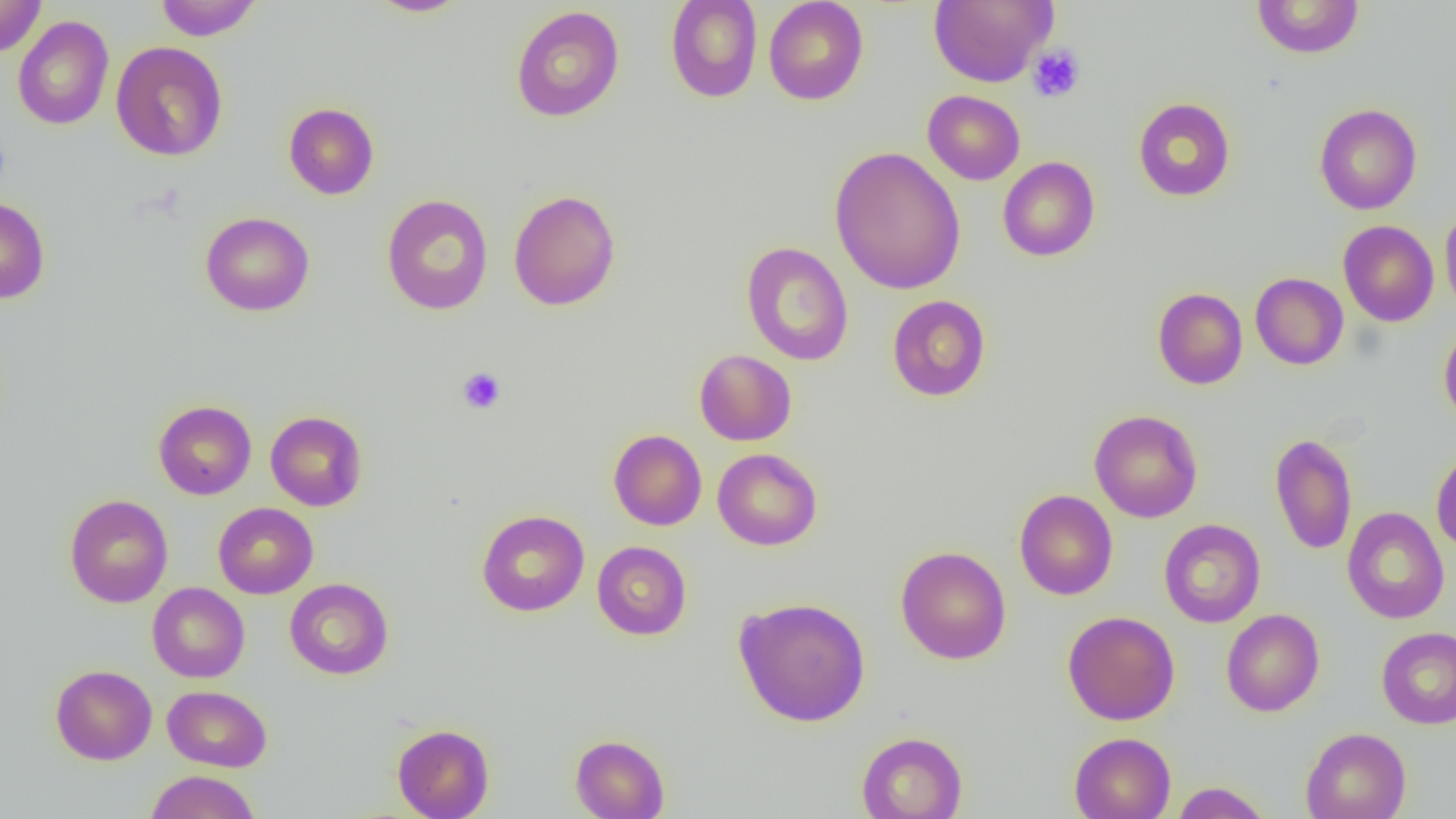
Summary:
  - Coordinate format: approximate bounding boxes as named x1/y1/x2/y2 corners in pixels
  - Uninfected red blood cell locations: (x1=0, y1=0, x2=46, y2=57), (x1=155, y1=0, x2=261, y2=41), (x1=365, y1=0, x2=472, y2=17), (x1=665, y1=0, x2=762, y2=103), (x1=763, y1=0, x2=869, y2=105), (x1=928, y1=0, x2=1057, y2=87), (x1=1251, y1=0, x2=1365, y2=59), (x1=510, y1=5, x2=625, y2=122), (x1=13, y1=15, x2=114, y2=129), (x1=110, y1=41, x2=228, y2=161), (x1=923, y1=90, x2=1025, y2=184), (x1=1133, y1=97, x2=1235, y2=202), (x1=283, y1=102, x2=379, y2=200), (x1=1314, y1=103, x2=1422, y2=214), (x1=829, y1=147, x2=966, y2=294), (x1=998, y1=157, x2=1100, y2=261), (x1=508, y1=189, x2=621, y2=311), (x1=381, y1=194, x2=494, y2=315), (x1=0, y1=197, x2=50, y2=304), (x1=1440, y1=203, x2=1456, y2=319), (x1=200, y1=212, x2=315, y2=316), (x1=1338, y1=220, x2=1439, y2=326), (x1=740, y1=241, x2=854, y2=366), (x1=1250, y1=272, x2=1348, y2=370), (x1=1152, y1=287, x2=1248, y2=389), (x1=887, y1=295, x2=991, y2=401), (x1=1439, y1=321, x2=1456, y2=426), (x1=694, y1=349, x2=797, y2=446), (x1=153, y1=400, x2=256, y2=500), (x1=1088, y1=409, x2=1203, y2=522), (x1=265, y1=411, x2=367, y2=511), (x1=608, y1=429, x2=707, y2=530), (x1=1269, y1=433, x2=1358, y2=555), (x1=712, y1=448, x2=822, y2=551), (x1=1431, y1=448, x2=1456, y2=555), (x1=1014, y1=489, x2=1118, y2=600), (x1=64, y1=494, x2=174, y2=608), (x1=213, y1=502, x2=318, y2=598), (x1=1342, y1=506, x2=1449, y2=624), (x1=476, y1=510, x2=590, y2=616), (x1=1159, y1=519, x2=1266, y2=628), (x1=592, y1=541, x2=692, y2=640), (x1=896, y1=545, x2=1011, y2=665), (x1=284, y1=578, x2=394, y2=680), (x1=147, y1=582, x2=250, y2=683), (x1=734, y1=596, x2=871, y2=727), (x1=1221, y1=609, x2=1324, y2=716), (x1=1062, y1=610, x2=1180, y2=725), (x1=1376, y1=626, x2=1456, y2=729), (x1=50, y1=664, x2=157, y2=765), (x1=162, y1=685, x2=272, y2=772), (x1=392, y1=723, x2=495, y2=818), (x1=1300, y1=727, x2=1411, y2=819), (x1=856, y1=731, x2=968, y2=819), (x1=1069, y1=732, x2=1176, y2=819), (x1=570, y1=734, x2=669, y2=818), (x1=145, y1=770, x2=260, y2=819), (x1=1170, y1=781, x2=1272, y2=818)
  - Platelet locations: (x1=1027, y1=44, x2=1086, y2=103), (x1=457, y1=367, x2=507, y2=414)
  - Slide-level diagnosis: no evidence of blood parasites
  - Preparation: thin blood smear
  - Field of view: one of a larger specimen
  - Magnification: 1000x
  - Modality: optical microscopy
  - Image size: 1456×819 pixels